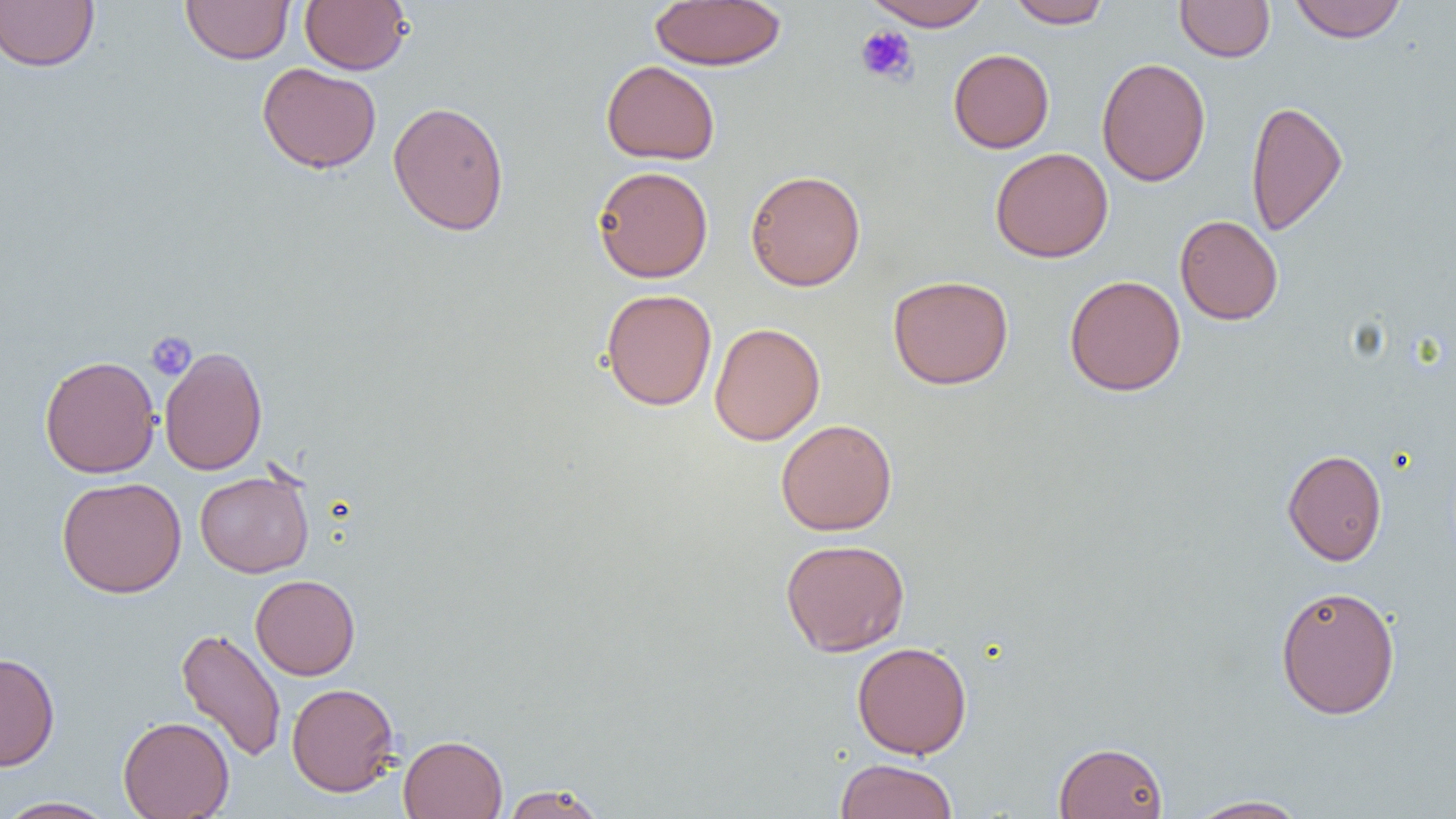 Approximate bounding boxes as named x1/y1/x2/y2 corners in pixels. Uninfected red blood cell locations: (x1=0, y1=0, x2=99, y2=72), (x1=181, y1=0, x2=295, y2=65), (x1=299, y1=0, x2=411, y2=75), (x1=864, y1=0, x2=991, y2=31), (x1=1006, y1=0, x2=1112, y2=28), (x1=1289, y1=0, x2=1407, y2=43), (x1=649, y1=1, x2=786, y2=70), (x1=1175, y1=1, x2=1275, y2=62), (x1=948, y1=48, x2=1054, y2=153), (x1=1096, y1=57, x2=1211, y2=186), (x1=601, y1=60, x2=721, y2=165), (x1=257, y1=63, x2=381, y2=173), (x1=1245, y1=99, x2=1348, y2=237), (x1=387, y1=100, x2=509, y2=236), (x1=990, y1=148, x2=1113, y2=263), (x1=593, y1=166, x2=713, y2=283), (x1=744, y1=169, x2=866, y2=291), (x1=1175, y1=214, x2=1283, y2=325), (x1=887, y1=275, x2=1014, y2=389), (x1=1064, y1=275, x2=1187, y2=397), (x1=601, y1=288, x2=717, y2=411), (x1=709, y1=322, x2=825, y2=445), (x1=159, y1=346, x2=268, y2=476), (x1=39, y1=355, x2=160, y2=478), (x1=776, y1=419, x2=898, y2=536), (x1=1282, y1=449, x2=1387, y2=565), (x1=195, y1=469, x2=314, y2=577), (x1=56, y1=476, x2=186, y2=598), (x1=780, y1=538, x2=910, y2=657), (x1=250, y1=574, x2=360, y2=680), (x1=1275, y1=585, x2=1401, y2=719), (x1=176, y1=627, x2=286, y2=763), (x1=852, y1=641, x2=972, y2=759), (x1=0, y1=652, x2=60, y2=771), (x1=286, y1=683, x2=399, y2=797), (x1=118, y1=715, x2=234, y2=819), (x1=398, y1=734, x2=508, y2=818), (x1=1054, y1=741, x2=1168, y2=819), (x1=835, y1=758, x2=958, y2=819), (x1=500, y1=783, x2=607, y2=819), (x1=1184, y1=795, x2=1312, y2=818), (x1=0, y1=796, x2=117, y2=818). Platelet locations: (x1=855, y1=24, x2=917, y2=85), (x1=146, y1=331, x2=197, y2=381). Slide-level diagnosis: negative for blood parasites. Captured at 1000x magnification. One field of a larger specimen. Optical microscopy. Thin blood smear. Image is 1456×819 pixels.